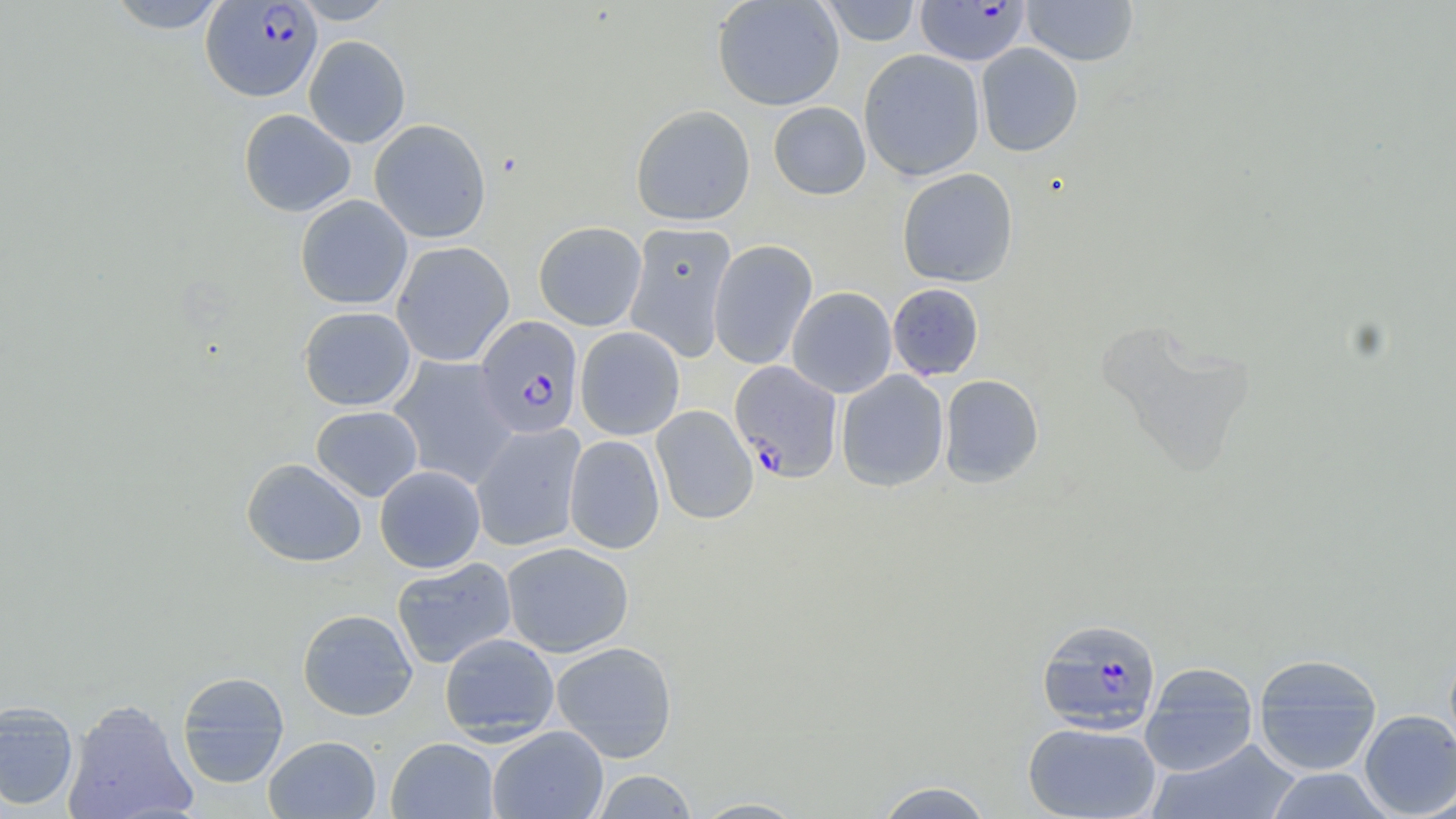
Approximate bounding boxes as (x1,y1)-(x2,y2) corner pairs in pixels. Uninfected red blood cell locations: (106,0)-(228,33), (290,0)-(398,24), (712,0)-(845,111), (818,1)-(922,46), (1021,1)-(1139,66), (303,35)-(411,148), (976,43)-(1084,157), (859,48)-(985,181), (768,101)-(871,200), (630,104)-(756,226), (239,108)-(356,217), (369,119)-(491,243), (897,168)-(1019,287), (295,194)-(412,310), (533,221)-(647,331), (623,222)-(738,362), (708,239)-(818,370), (391,241)-(514,366), (887,283)-(984,381), (787,287)-(897,398), (299,306)-(416,411), (1096,320)-(1260,477), (575,326)-(685,440), (388,356)-(519,489), (836,370)-(949,492), (939,374)-(1044,487), (311,405)-(423,502), (651,405)-(758,525), (471,423)-(585,552), (564,434)-(665,554), (241,458)-(367,567), (374,465)-(486,573), (501,541)-(634,657), (392,557)-(517,669), (297,608)-(417,720), (439,633)-(559,743), (550,641)-(678,762), (1252,653)-(1383,775), (1140,662)-(1259,776), (176,671)-(290,788), (62,699)-(197,819), (0,701)-(79,812), (1358,709)-(1455,818), (1022,721)-(1162,818), (488,726)-(609,819), (264,735)-(381,818), (386,737)-(499,819), (1148,739)-(1303,819), (1263,768)-(1393,818), (591,769)-(700,818), (871,780)-(995,818), (690,797)-(809,818). Plasmodium falciparum-infected red blood cell locations: (201,1)-(321,102), (915,1)-(1031,66), (475,316)-(584,438), (729,360)-(843,483), (1036,617)-(1162,735). Slide-level diagnosis: Plasmodium falciparum. Captured at 1000x magnification. May-Grünwald-Giemsa stain. Image is 1456×819 pixels. One field of a larger specimen. Optical microscopy. Thin blood smear.